Name the cell type shown.
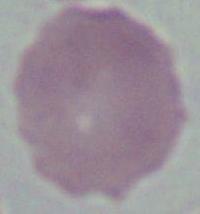
An erythrocyte.

magnification = 1000x
modality = photomicrograph